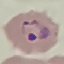

Result: malaria parasites detected. Cell patch, automatically extracted from a larger field of view and resized to 64 × 64 pixels. Giemsa-stained preparation. Thin blood smear. Acquired by smartphone through the microscope eyepiece.